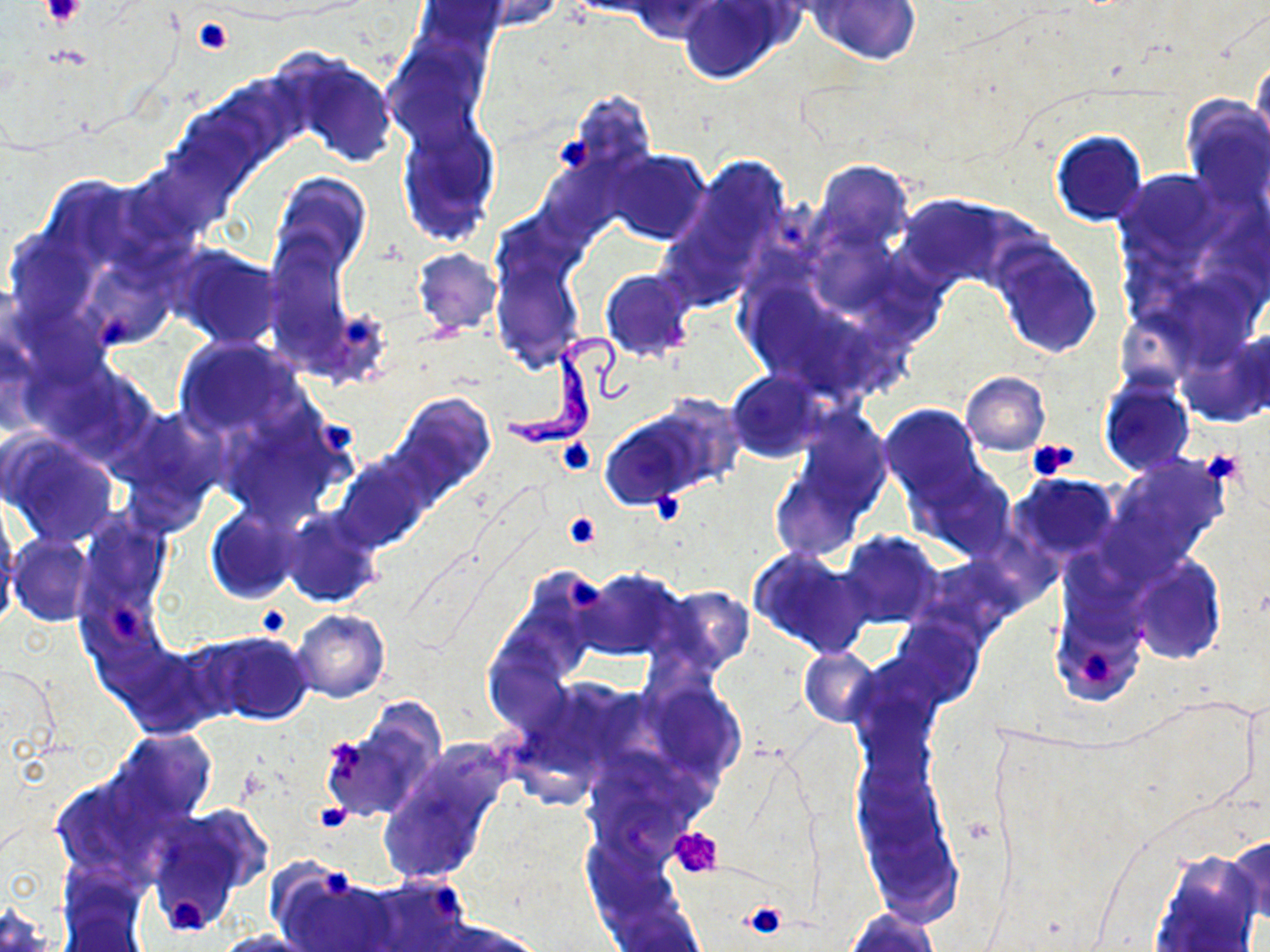 Approximate bounding boxes as (x1,y1)-(x2,y2) corner pairs in pixels. Trypanosoma brucei locations: (504,334)-(638,450). Platelet locations: (42,1)-(85,27), (192,16)-(234,56), (555,133)-(597,172), (99,315)-(137,345), (342,316)-(377,345), (323,424)-(356,456), (557,437)-(596,475), (1027,438)-(1080,480), (1206,451)-(1241,486), (654,488)-(684,526), (562,510)-(602,549), (566,576)-(603,612), (109,605)-(144,645), (256,607)-(292,638), (1080,649)-(1115,686), (323,738)-(366,775), (312,800)-(353,831), (669,827)-(723,879), (321,865)-(353,899), (428,886)-(462,913), (161,893)-(207,935), (743,901)-(786,939). Uninfected red blood cell locations: (473,0)-(563,32), (810,0)-(922,66), (413,1)-(505,63), (630,1)-(720,41), (676,1)-(790,85), (386,41)-(487,143), (1250,53)-(1270,156), (288,55)-(397,168), (562,90)-(658,182), (1182,97)-(1270,209), (397,115)-(501,243), (1050,130)-(1147,227), (604,150)-(711,246), (686,153)-(790,264), (813,159)-(913,256), (537,160)-(620,242), (1122,169)-(1222,261), (271,173)-(372,277), (897,193)-(1019,298), (5,229)-(97,328), (490,237)-(582,369), (265,239)-(352,356), (992,243)-(1103,360), (167,245)-(281,348), (413,249)-(501,335), (82,254)-(176,349), (600,270)-(695,361), (318,308)-(393,389), (174,336)-(306,445), (1181,337)-(1268,426), (727,370)-(827,462), (961,372)-(1050,455), (1099,380)-(1194,476), (395,393)-(495,492), (600,402)-(725,506), (880,404)-(982,503), (120,406)-(225,514), (217,411)-(348,523), (795,412)-(890,517), (3,435)-(119,547), (334,454)-(433,551), (1110,455)-(1230,565), (770,462)-(868,562), (912,463)-(1016,560), (1012,475)-(1118,559), (205,507)-(300,604), (282,509)-(382,608), (76,511)-(170,629), (0,513)-(19,616), (841,531)-(941,629), (8,534)-(93,626), (748,548)-(874,657), (1131,557)-(1225,663), (579,569)-(685,660), (663,586)-(755,670), (1052,595)-(1146,706), (293,609)-(390,702), (892,620)-(983,707), (203,631)-(312,725), (484,640)-(574,736), (110,641)-(216,734), (799,647)-(881,727), (647,685)-(746,778), (331,698)-(448,822), (109,728)-(216,824), (378,758)-(502,884), (51,775)-(178,882), (144,810)-(265,930), (1227,835)-(1270,923), (1150,854)-(1260,952), (276,866)-(400,952), (57,869)-(150,950), (362,875)-(471,952), (0,903)-(55,951), (845,908)-(939,951), (432,919)-(545,951), (213,929)-(319,952). Slide-level diagnosis: Trypanosoma brucei. Image is 1270×952 pixels. Thin blood smear. May-Grünwald-Giemsa-stained preparation. Light microscopy. Captured at 1000x magnification. Single field of view.